Identify the parasite.
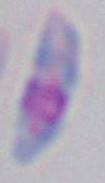
Toxoplasma gondii.

modality = micrograph
magnification = 1000x